Assess for parasitized red blood cells.
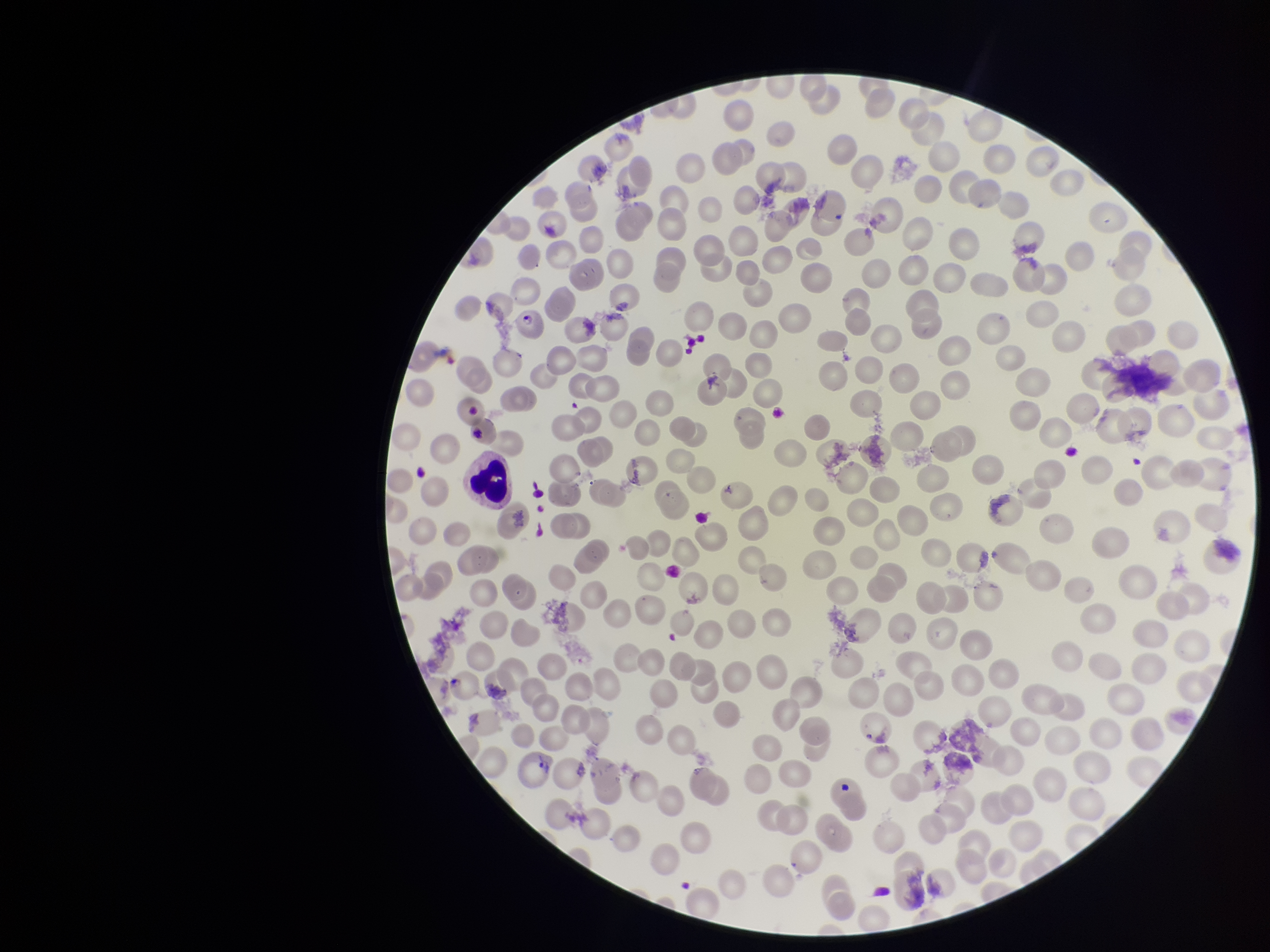
Detected.

Red blood cell count: 249. Preparation: thin. Species reported for this patient: Plasmodium vivax. Single field of view. Parasitized red blood cell count: 1. Photographed through the microscope eyepiece with a smartphone camera. Patient malaria status: positive. Giemsa stain. Image is 1270×952 pixels.